Identify the parasite.
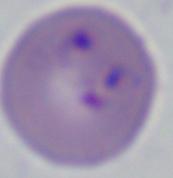

Babesia.

magnification = 1000x
modality = micrograph